Assess this cell for malaria.
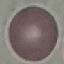
It is uninfected.

Summary:
  - Stain: Giemsa
  - Image type: cell patch, automatically extracted from a larger field of view and resized to 64 × 64 pixels
  - Capture: smartphone through the microscope eyepiece
  - Preparation: thin blood smear